Assess this cell for malaria.
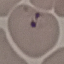

Parasitized.

Automatically extracted cell patch, resized to 64 × 64 pixels. Giemsa-stained preparation. Photographed with a smartphone camera at the microscope eyepiece. Thin smear of blood.